State which parasite is depicted.
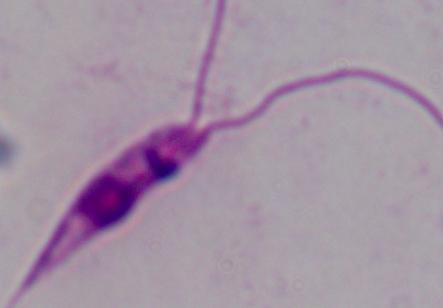
This is Leishmania.

Summary:
  - Magnification: 1000x
  - Modality: photomicrograph